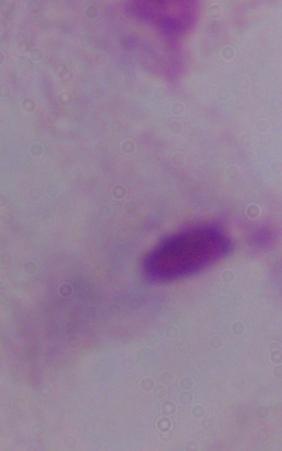 Micrograph. A trichomonad is seen. 1000x magnification.